Assess this cell for malaria.
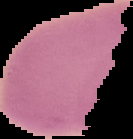

Uninfected.

From a thin blood smear. Cell region segmented out of the field of view; the surrounding area is masked to black. Image is 133×139 pixels.